Name the parasite shown.
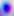

Toxoplasma gondii.

400x magnification. Photomicrograph.